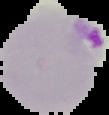
Malaria status: parasitized. Cell region segmented out of the field of view; the surrounding area is masked to black. Image is 109×115 pixels. From a thin blood film.